Identify the cell.
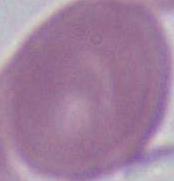

An erythrocyte.

magnification = 1000x
modality = photomicrograph